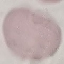
{
  "result": "negative for malaria parasites",
  "image_type": "automatically extracted cell patch, resized to 64 × 64 pixels",
  "stain": "Giemsa",
  "capture": "smartphone camera at the microscope eyepiece",
  "preparation": "thin blood film"
}